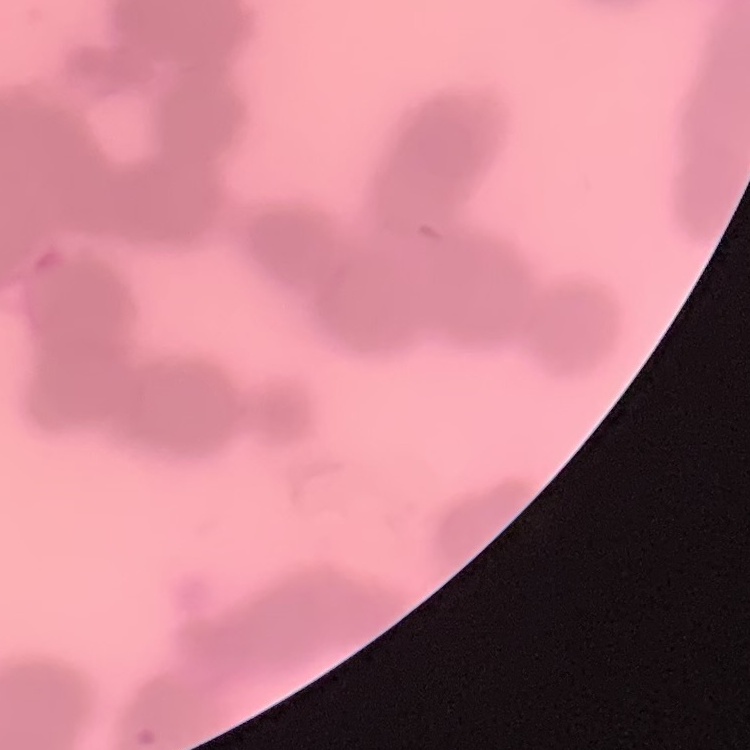

The red blood cells exhibit rouleaux formation. Square crop of a larger photomicrograph. Thin peripheral smear. Stained with either Field's or Giemsa.